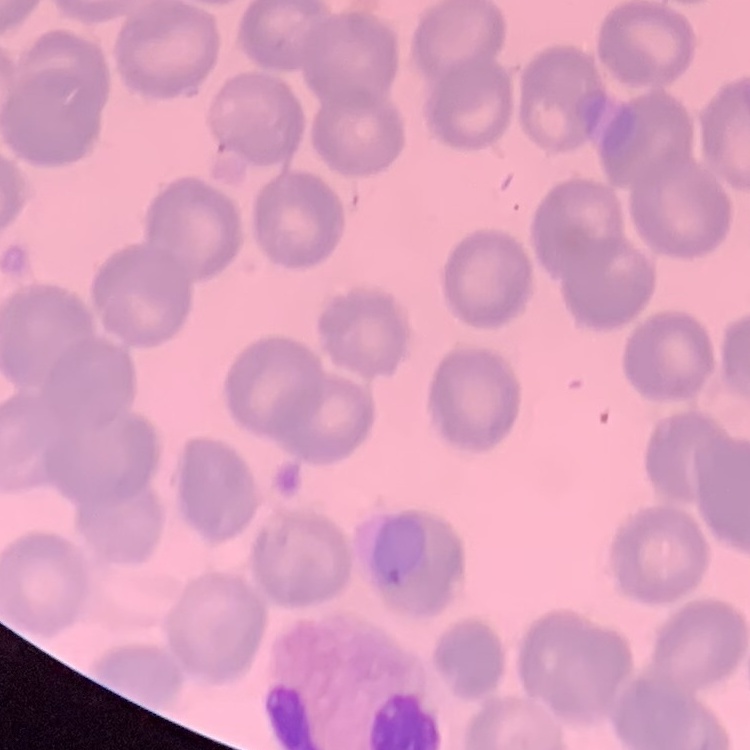 The red blood cells exhibit no rouleaux formation. Thin blood film. Square crop of a larger photomicrograph. Field's or Giemsa stain.